Give the position of every Plasmodium parasite visible.
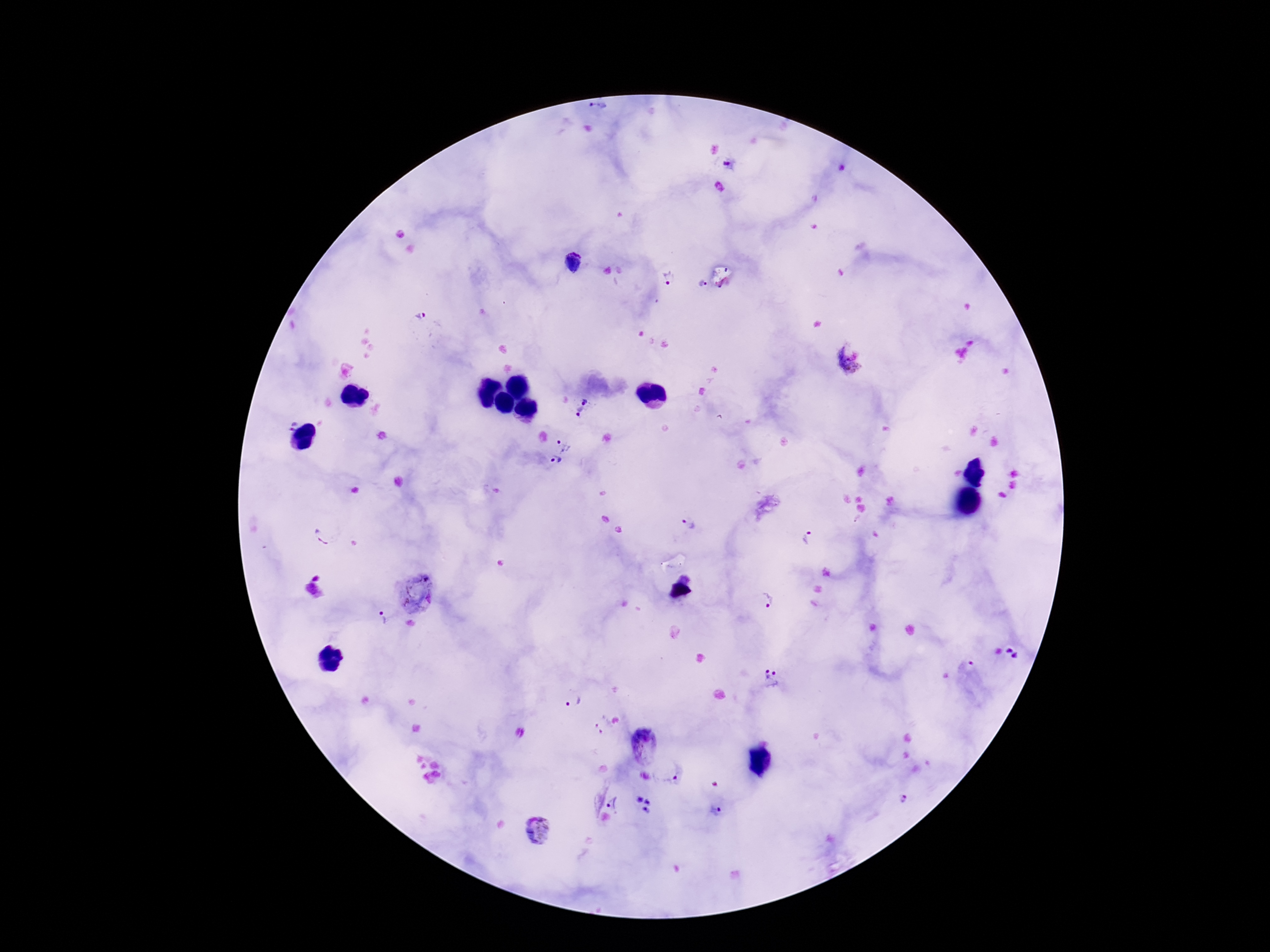
Approximate centers as {x, y} in pixels.
Plasmodium parasites: {600, 112}, {730, 165}, {669, 279}, {702, 282}, {422, 316}, {846, 363}, {587, 401}, {577, 416}, {564, 445}, {556, 463}, {689, 526}, {323, 538}, {809, 538}, {415, 592}, {769, 601}, {380, 619}, {1013, 653}, {771, 678}, {576, 700}, {604, 727}, {643, 743}, {667, 770}, {903, 797}, {615, 804}, {717, 811}, {537, 831}.

Patient malaria status: infected. Giemsa stain. One field from this slide. 100x magnification. Image is 1270×952 pixels. Thick peripheral-blood smear. Photographed through the microscope eyepiece with a smartphone camera.